Assess the morphology of the erythrocytes.
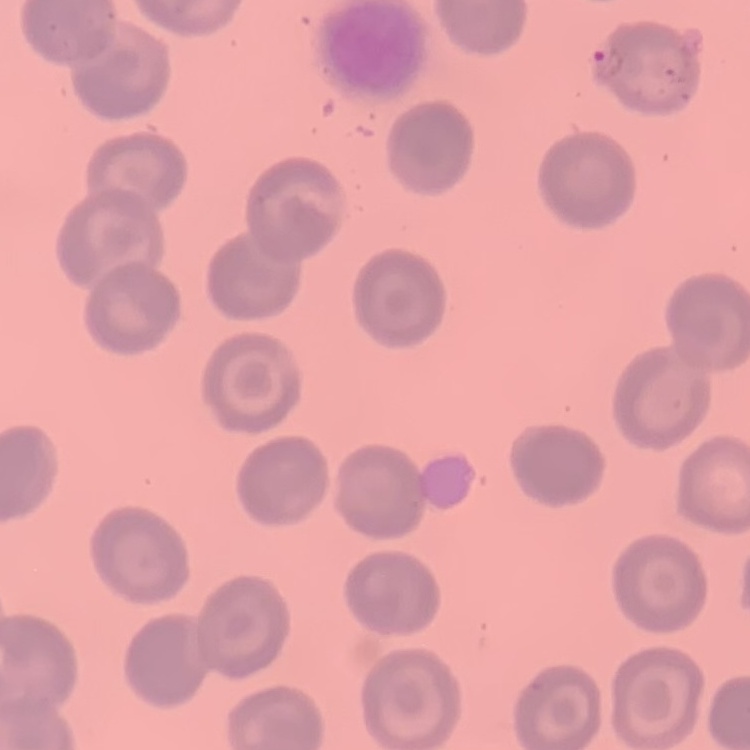

No rouleaux formation.

Thin peripheral smear. One tile cut from a larger photomicrograph. Field's or Giemsa stain.